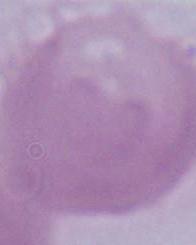
modality = photomicrograph
magnification = 1000x
identification = red blood cell